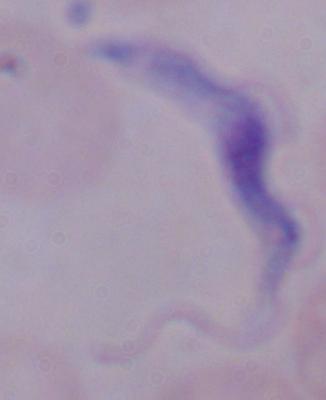
Summary:
  - Modality: micrograph
  - Identification: trypanosome
  - Magnification: 1000x